Classify this cell by malaria status.
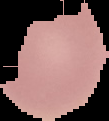
It is uninfected.

image size = 109×121 pixels
preparation = thin blood film
image type = segmented cell region with the area outside set to black